Name the cell type shown.
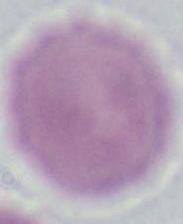
This is an erythrocyte.

Summary:
  - Magnification: 1000x
  - Modality: micrograph